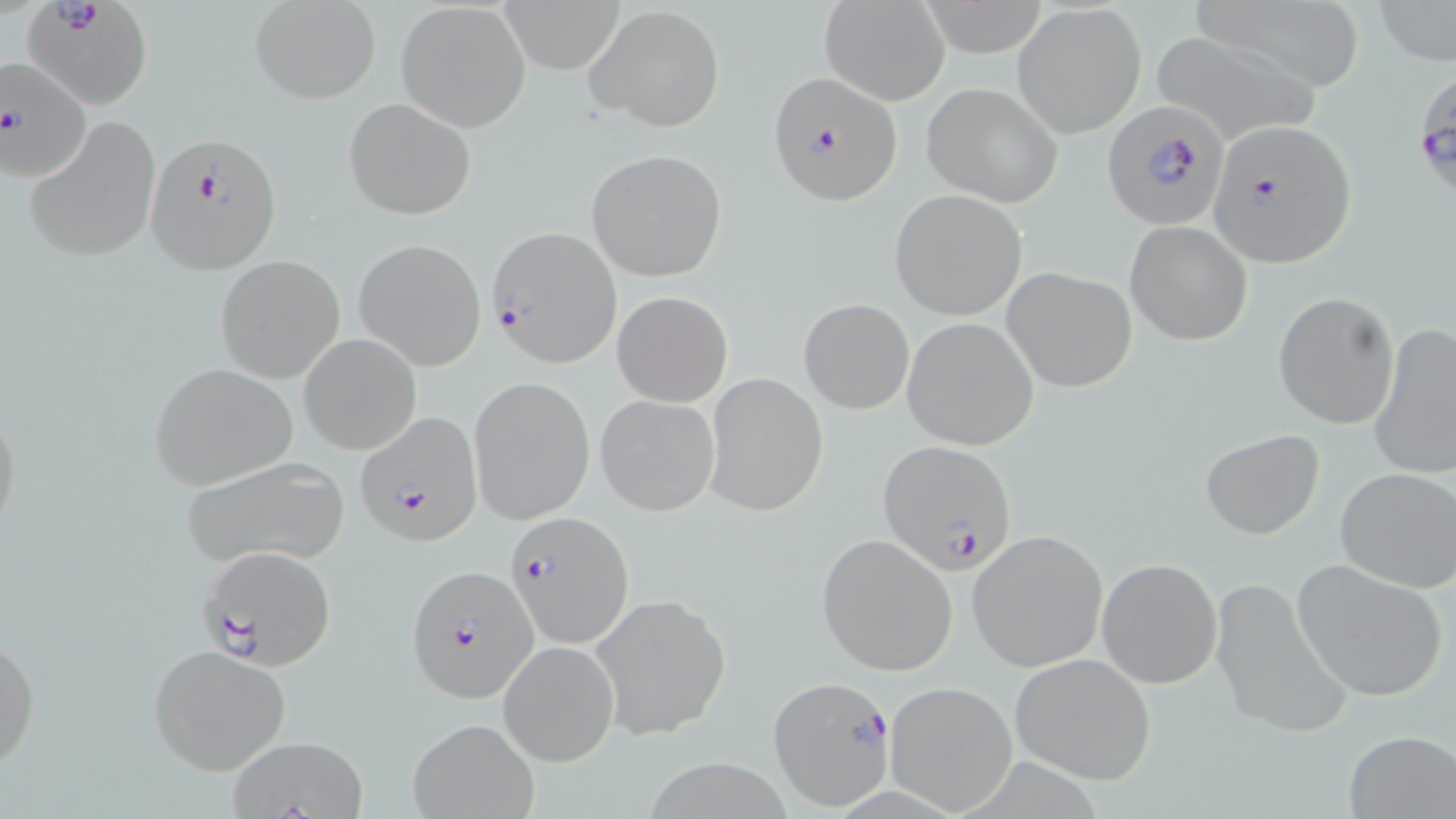

Summary:
  - Coordinate format: approximate bounding boxes as (x1,y1)-(x2,y2) corner pairs in pixels
  - Uninfected red blood cell locations: (499,0)-(627,72), (1372,0)-(1456,68), (819,1)-(950,106), (249,2)-(380,104), (396,2)-(530,132), (1014,3)-(1146,137), (586,5)-(726,132), (1150,30)-(1317,146), (923,83)-(1063,205), (343,97)-(476,220), (27,115)-(161,263), (586,149)-(729,283), (889,188)-(1026,320), (1125,221)-(1253,347), (355,237)-(486,370), (215,255)-(347,384), (1002,267)-(1137,391), (612,291)-(732,407), (1273,291)-(1401,429), (799,298)-(914,414), (903,317)-(1039,449), (1369,323)-(1456,481), (299,334)-(421,456), (148,362)-(298,489), (704,373)-(827,517), (469,375)-(595,526), (596,394)-(720,517), (0,401)-(24,547), (1199,429)-(1325,539), (179,457)-(350,569), (1336,468)-(1456,592), (966,529)-(1108,672), (816,534)-(957,675), (1096,557)-(1223,690), (1292,558)-(1450,702), (1211,577)-(1351,740), (589,594)-(731,739), (0,625)-(39,776), (499,640)-(619,767), (147,643)-(295,775), (1009,652)-(1156,785), (885,681)-(1019,815), (407,718)-(539,818), (1343,729)-(1456,817), (224,734)-(370,818)
  - Plasmodium falciparum-infected red blood cell locations: (23,0)-(152,111), (0,56)-(91,184), (767,71)-(903,206), (1417,82)-(1455,204), (1102,101)-(1229,230), (1209,119)-(1358,267), (145,130)-(284,273), (487,226)-(623,366), (356,415)-(482,547), (879,439)-(1018,577), (506,511)-(633,649), (197,545)-(338,668), (407,564)-(538,703), (768,676)-(895,809)
  - Slide-level diagnosis: Plasmodium falciparum
  - Preparation: thin blood film
  - Image size: 1456×819 pixels
  - Modality: optical microscopy
  - Field of view: single
  - Magnification: 1000x
  - Stain: May-Grünwald-Giemsa